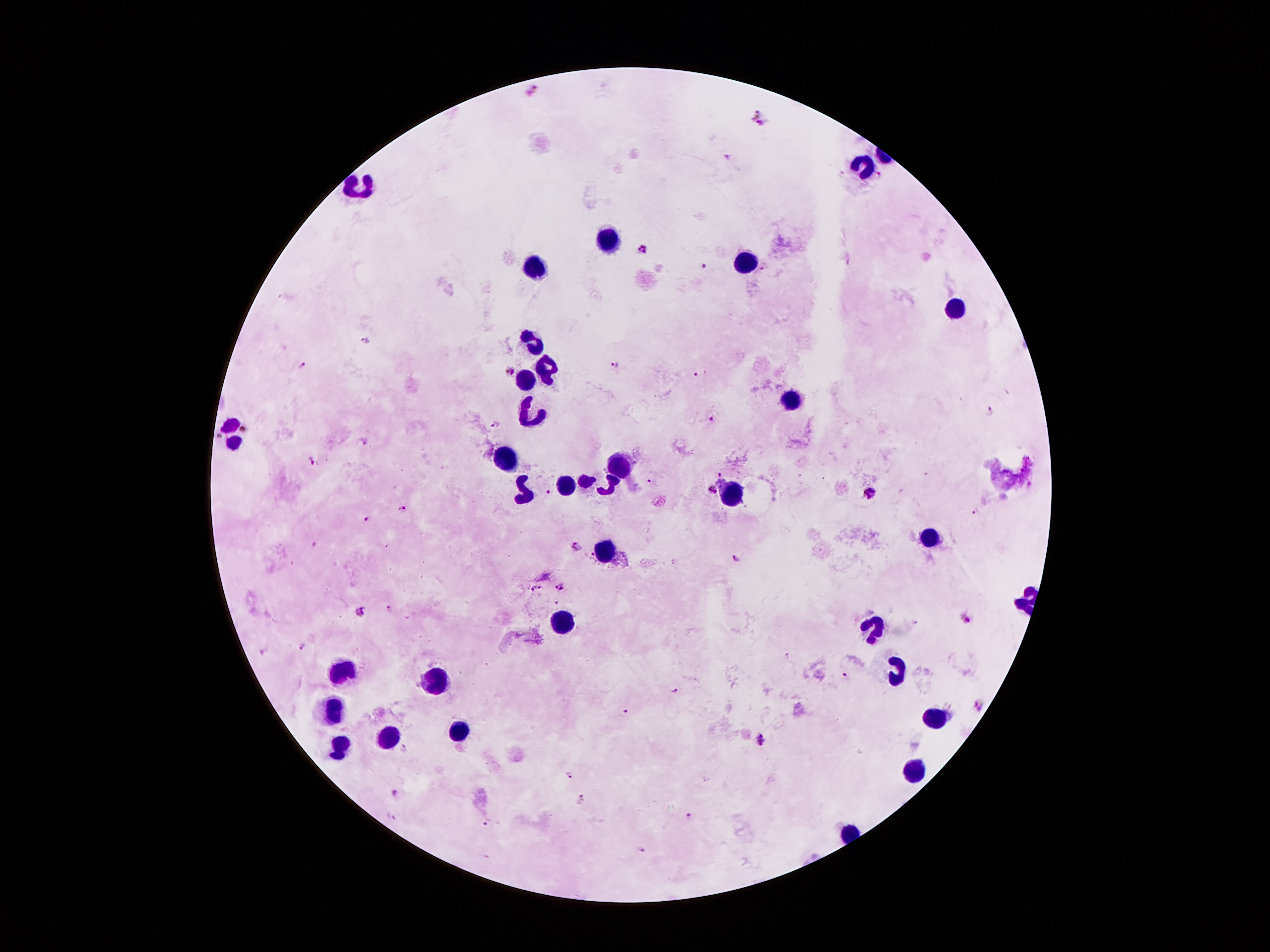 Approximate object centers, in pixels from the top-left corner. Leukocyte locations: (x=868, y=164), (x=362, y=185), (x=604, y=239), (x=746, y=262), (x=534, y=267), (x=952, y=305), (x=534, y=344), (x=547, y=367), (x=526, y=382), (x=791, y=403), (x=530, y=416), (x=230, y=433), (x=509, y=458), (x=618, y=466), (x=600, y=483), (x=560, y=485), (x=528, y=491), (x=730, y=494), (x=927, y=536), (x=606, y=550), (x=564, y=620), (x=875, y=624), (x=344, y=670), (x=896, y=670), (x=432, y=682), (x=327, y=706), (x=935, y=718), (x=455, y=731), (x=390, y=735), (x=341, y=750), (x=917, y=771). Malaria parasite locations: (x=532, y=90), (x=758, y=115), (x=728, y=157), (x=879, y=175), (x=642, y=248), (x=704, y=265), (x=766, y=267), (x=363, y=338), (x=614, y=363), (x=304, y=364), (x=698, y=371), (x=510, y=372), (x=992, y=412), (x=708, y=418), (x=495, y=425), (x=364, y=442), (x=311, y=460), (x=720, y=471), (x=650, y=480), (x=1028, y=481), (x=713, y=490), (x=548, y=491), (x=871, y=493), (x=400, y=507), (x=976, y=511), (x=366, y=517), (x=314, y=543), (x=735, y=557), (x=560, y=587), (x=536, y=589), (x=388, y=608), (x=360, y=613), (x=913, y=620), (x=966, y=621), (x=302, y=646), (x=263, y=651), (x=789, y=656), (x=846, y=675), (x=675, y=689), (x=981, y=704), (x=624, y=712), (x=760, y=738), (x=405, y=747), (x=570, y=774), (x=396, y=794), (x=582, y=797), (x=687, y=815), (x=393, y=817), (x=488, y=822), (x=642, y=849). Single field of view. Giemsa stain. 100x magnification. Photographed through the microscope eyepiece with a smartphone camera. Image is 1270×952 pixels. Patient malaria status: positive for Plasmodium falciparum. Thick blood film.